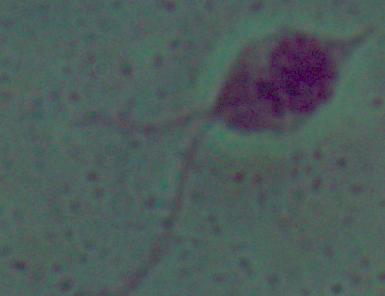 A Leishmania parasite is seen. Micrograph. 1000x magnification.